Outline each blood parasite and name the species.
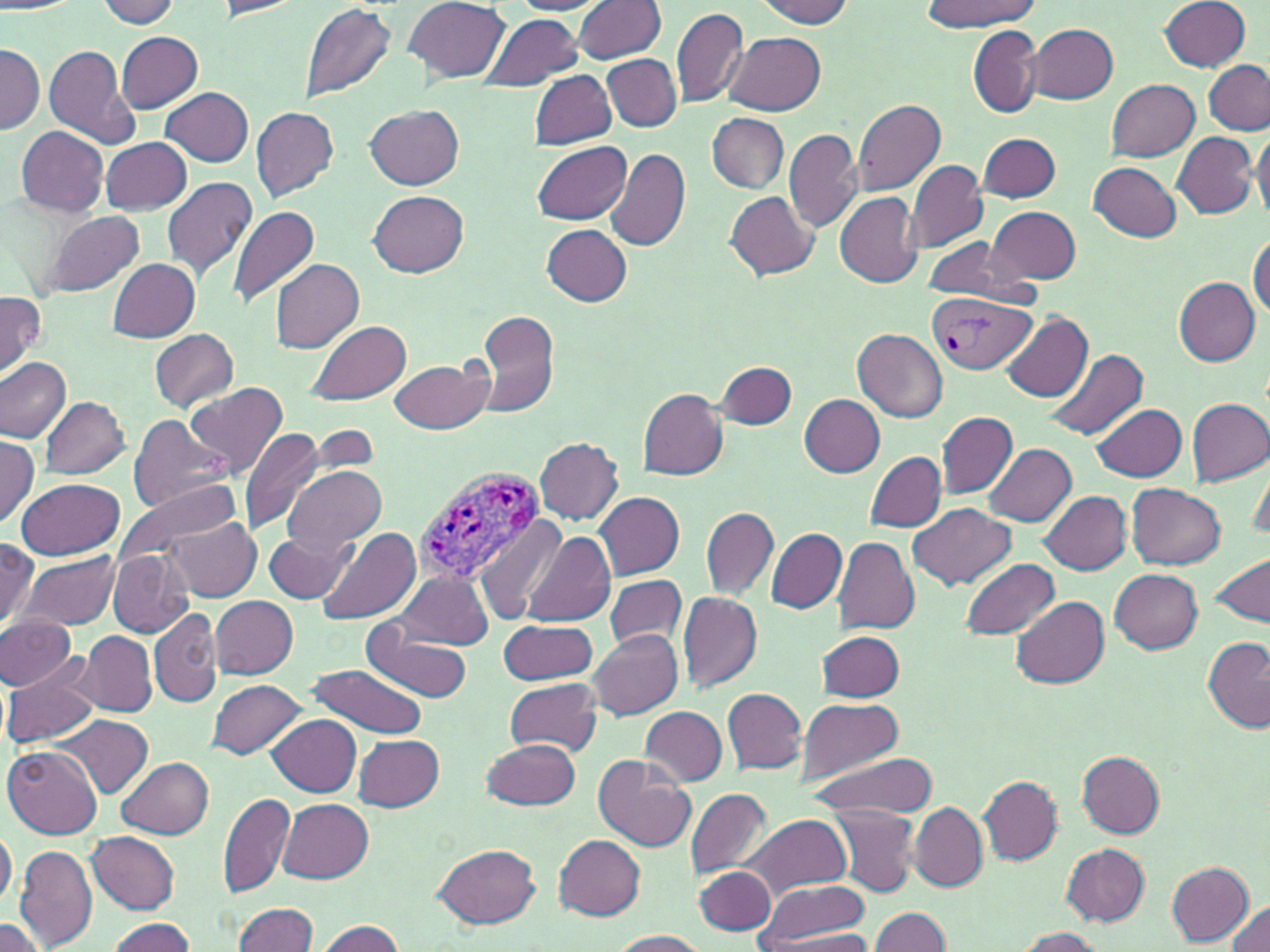

Approximate bounding boxes as named x1/y1/x2/y2 corners in pixels.
Plasmodium vivax-infected red blood cells: (x1=927, y1=292, x2=1034, y2=374), (x1=412, y1=466, x2=547, y2=584).
No Plasmodium falciparum, Plasmodium ovale, Plasmodium malariae, Babesia divergens, or Trypanosoma brucei observed.

Summary:
  - Uninfected red blood cell locations: (x1=97, y1=0, x2=180, y2=28), (x1=403, y1=0, x2=510, y2=83), (x1=511, y1=0, x2=609, y2=15), (x1=756, y1=0, x2=854, y2=26), (x1=1160, y1=0, x2=1252, y2=72), (x1=212, y1=1, x2=302, y2=20), (x1=574, y1=1, x2=666, y2=63), (x1=918, y1=1, x2=1037, y2=31), (x1=299, y1=2, x2=397, y2=103), (x1=671, y1=8, x2=748, y2=107), (x1=483, y1=14, x2=582, y2=90), (x1=1027, y1=23, x2=1118, y2=102), (x1=968, y1=25, x2=1042, y2=119), (x1=726, y1=31, x2=824, y2=115), (x1=115, y1=32, x2=204, y2=112), (x1=1, y1=43, x2=42, y2=133), (x1=44, y1=45, x2=142, y2=150), (x1=602, y1=54, x2=682, y2=130), (x1=1202, y1=61, x2=1270, y2=135), (x1=531, y1=70, x2=617, y2=149), (x1=1104, y1=78, x2=1200, y2=162), (x1=160, y1=87, x2=253, y2=166), (x1=853, y1=98, x2=945, y2=197), (x1=250, y1=105, x2=339, y2=202), (x1=365, y1=105, x2=462, y2=190), (x1=709, y1=114, x2=788, y2=193), (x1=16, y1=125, x2=108, y2=217), (x1=784, y1=129, x2=863, y2=232), (x1=1251, y1=131, x2=1270, y2=218), (x1=979, y1=132, x2=1060, y2=202), (x1=1172, y1=132, x2=1258, y2=218), (x1=101, y1=137, x2=191, y2=215), (x1=531, y1=141, x2=632, y2=226), (x1=606, y1=146, x2=690, y2=252), (x1=905, y1=160, x2=989, y2=254), (x1=1090, y1=163, x2=1180, y2=241), (x1=161, y1=177, x2=258, y2=282), (x1=370, y1=190, x2=469, y2=277), (x1=725, y1=191, x2=818, y2=279), (x1=835, y1=193, x2=922, y2=287), (x1=228, y1=206, x2=322, y2=306), (x1=988, y1=206, x2=1082, y2=285), (x1=43, y1=210, x2=145, y2=299), (x1=541, y1=225, x2=632, y2=306), (x1=1249, y1=233, x2=1270, y2=319), (x1=922, y1=237, x2=1026, y2=303), (x1=106, y1=257, x2=201, y2=342), (x1=270, y1=258, x2=365, y2=353), (x1=1174, y1=277, x2=1259, y2=367), (x1=0, y1=291, x2=46, y2=380), (x1=477, y1=308, x2=562, y2=420), (x1=999, y1=312, x2=1092, y2=402), (x1=307, y1=320, x2=412, y2=403), (x1=150, y1=329, x2=239, y2=411), (x1=852, y1=329, x2=947, y2=421), (x1=1046, y1=347, x2=1147, y2=441), (x1=0, y1=357, x2=71, y2=444), (x1=389, y1=357, x2=494, y2=435), (x1=718, y1=361, x2=796, y2=429), (x1=186, y1=382, x2=287, y2=478), (x1=638, y1=388, x2=728, y2=479), (x1=799, y1=394, x2=885, y2=477), (x1=1185, y1=396, x2=1270, y2=485), (x1=40, y1=397, x2=129, y2=480), (x1=1091, y1=403, x2=1186, y2=480), (x1=937, y1=410, x2=1017, y2=499), (x1=127, y1=414, x2=232, y2=515), (x1=239, y1=429, x2=329, y2=536), (x1=0, y1=435, x2=41, y2=530), (x1=535, y1=438, x2=623, y2=524), (x1=984, y1=442, x2=1075, y2=526), (x1=866, y1=452, x2=945, y2=532), (x1=1249, y1=456, x2=1270, y2=542), (x1=284, y1=465, x2=386, y2=556), (x1=16, y1=477, x2=124, y2=560), (x1=113, y1=480, x2=243, y2=573), (x1=1128, y1=484, x2=1224, y2=570), (x1=1040, y1=490, x2=1133, y2=575), (x1=595, y1=491, x2=685, y2=579), (x1=908, y1=504, x2=1016, y2=591), (x1=701, y1=506, x2=777, y2=601), (x1=473, y1=515, x2=570, y2=626), (x1=166, y1=519, x2=260, y2=601), (x1=319, y1=528, x2=421, y2=628), (x1=766, y1=528, x2=847, y2=614), (x1=523, y1=531, x2=615, y2=626), (x1=263, y1=532, x2=352, y2=603), (x1=834, y1=535, x2=920, y2=632), (x1=1, y1=539, x2=39, y2=629), (x1=21, y1=550, x2=121, y2=630), (x1=108, y1=550, x2=194, y2=636), (x1=1210, y1=554, x2=1269, y2=627), (x1=960, y1=558, x2=1059, y2=639), (x1=1109, y1=568, x2=1203, y2=653), (x1=394, y1=570, x2=493, y2=649), (x1=603, y1=573, x2=687, y2=653), (x1=678, y1=591, x2=763, y2=693), (x1=1011, y1=594, x2=1108, y2=688), (x1=211, y1=596, x2=298, y2=680), (x1=149, y1=607, x2=221, y2=708), (x1=0, y1=615, x2=75, y2=691), (x1=0, y1=618, x2=148, y2=700), (x1=498, y1=621, x2=598, y2=686), (x1=363, y1=627, x2=476, y2=703), (x1=586, y1=628, x2=681, y2=720), (x1=77, y1=630, x2=157, y2=717), (x1=818, y1=630, x2=905, y2=703), (x1=1203, y1=636, x2=1270, y2=733), (x1=2, y1=662, x2=101, y2=750), (x1=306, y1=664, x2=426, y2=737), (x1=206, y1=678, x2=305, y2=760), (x1=503, y1=678, x2=603, y2=756), (x1=724, y1=688, x2=808, y2=773), (x1=796, y1=698, x2=906, y2=782), (x1=640, y1=706, x2=727, y2=786), (x1=267, y1=714, x2=362, y2=797), (x1=56, y1=715, x2=153, y2=797), (x1=355, y1=735, x2=445, y2=811), (x1=482, y1=737, x2=581, y2=809), (x1=3, y1=744, x2=103, y2=838), (x1=1077, y1=751, x2=1164, y2=837), (x1=594, y1=752, x2=697, y2=851), (x1=810, y1=755, x2=936, y2=817), (x1=117, y1=757, x2=213, y2=838), (x1=979, y1=775, x2=1063, y2=865), (x1=685, y1=787, x2=773, y2=879), (x1=219, y1=791, x2=295, y2=898), (x1=278, y1=798, x2=374, y2=882), (x1=909, y1=802, x2=987, y2=890), (x1=828, y1=804, x2=917, y2=897), (x1=742, y1=814, x2=850, y2=900), (x1=0, y1=824, x2=16, y2=911), (x1=88, y1=831, x2=180, y2=913), (x1=553, y1=834, x2=645, y2=922), (x1=431, y1=843, x2=540, y2=928), (x1=1060, y1=843, x2=1149, y2=925), (x1=15, y1=844, x2=98, y2=950), (x1=1165, y1=860, x2=1255, y2=945), (x1=694, y1=867, x2=775, y2=934), (x1=755, y1=879, x2=869, y2=947), (x1=1226, y1=900, x2=1270, y2=952), (x1=231, y1=901, x2=318, y2=952), (x1=869, y1=908, x2=951, y2=952), (x1=0, y1=917, x2=49, y2=952), (x1=107, y1=917, x2=197, y2=952), (x1=313, y1=919, x2=408, y2=952), (x1=1012, y1=927, x2=1104, y2=951), (x1=758, y1=929, x2=880, y2=951), (x1=607, y1=930, x2=709, y2=951)
  - Slide-level diagnosis: Plasmodium vivax
  - Field of view: one of a larger specimen
  - Image size: 1270×952 pixels
  - Stain: May-Grünwald-Giemsa
  - Magnification: 1000x
  - Modality: optical microscopy
  - Preparation: thin blood film